Locate and identify every blood parasite.
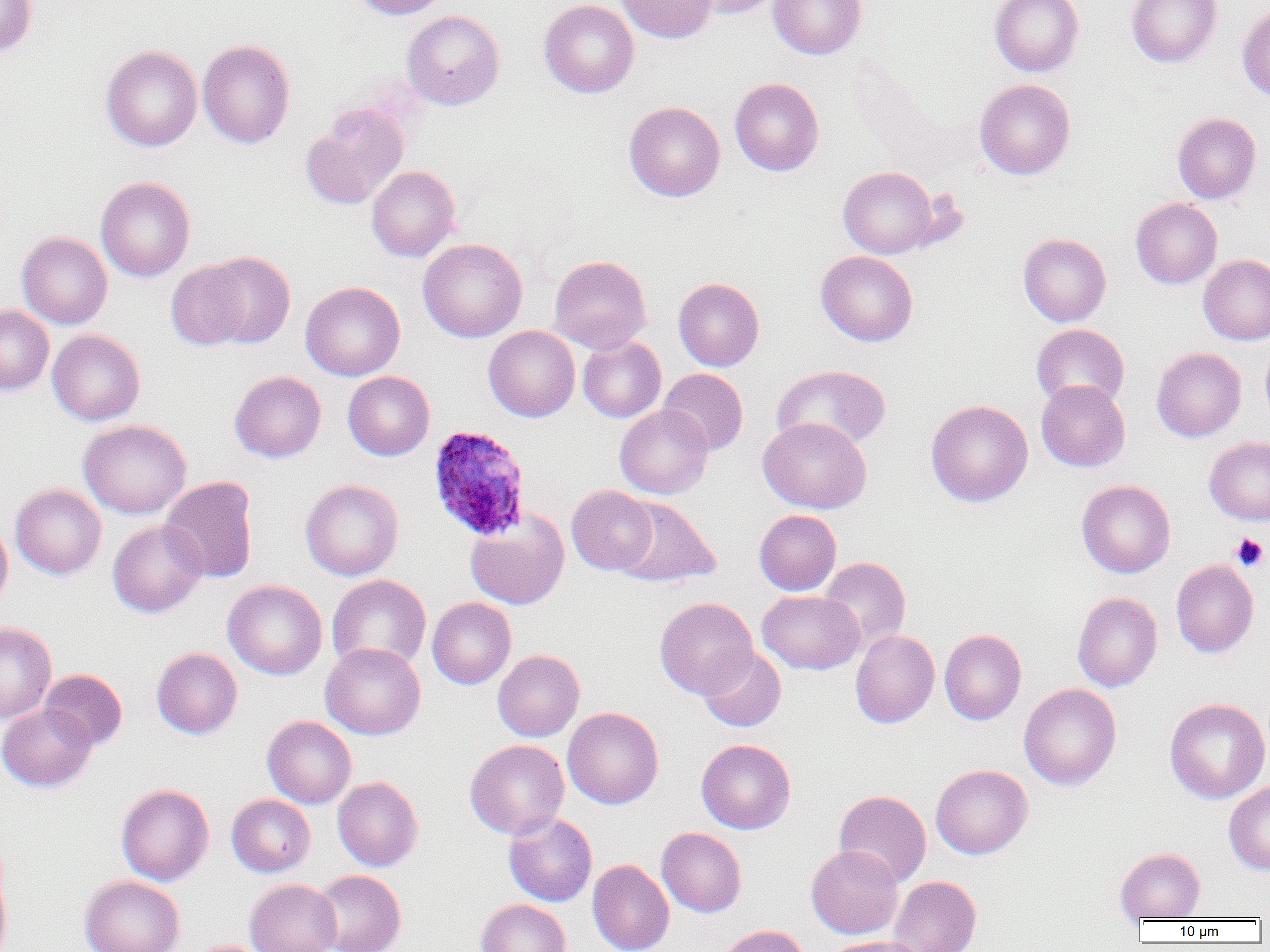
Approximate bounding boxes as (x1, y1, x2, y2) in pixels.
Plasmodium ovale-infected red blood cells: (427, 425, 532, 541).
No Plasmodium falciparum, Plasmodium malariae, Plasmodium vivax, Babesia divergens, or Trypanosoma brucei observed.

Summary:
  - Platelet locations: (1230, 532, 1269, 572)
  - Uninfected red blood cell locations: (0, 0, 37, 56), (351, 0, 451, 20), (539, 0, 639, 98), (615, 0, 717, 44), (684, 0, 783, 18), (768, 0, 866, 60), (989, 0, 1084, 77), (1126, 0, 1222, 68), (1237, 3, 1270, 102), (401, 10, 505, 110), (197, 39, 295, 149), (100, 44, 202, 152), (730, 77, 824, 176), (974, 78, 1075, 180), (624, 101, 725, 202), (301, 104, 409, 210), (1172, 112, 1261, 204), (367, 166, 460, 262), (838, 166, 941, 258), (95, 176, 195, 282), (1130, 198, 1222, 288), (16, 231, 112, 329), (1018, 233, 1111, 326), (418, 238, 527, 342), (816, 250, 918, 346), (196, 251, 296, 348), (1198, 254, 1270, 345), (549, 255, 651, 353), (165, 260, 255, 351), (673, 277, 764, 371), (300, 281, 405, 381), (0, 306, 54, 395), (1031, 324, 1129, 410), (483, 326, 580, 421), (47, 329, 145, 426), (578, 335, 666, 422), (1260, 340, 1270, 428), (1151, 346, 1246, 442), (772, 364, 891, 452), (658, 368, 748, 456), (229, 371, 326, 463), (343, 371, 435, 460), (1035, 379, 1130, 472), (925, 399, 1033, 507), (614, 405, 713, 499), (758, 417, 871, 513), (78, 419, 192, 519), (1204, 436, 1270, 525), (159, 476, 259, 583), (299, 478, 404, 581), (1076, 479, 1176, 578), (10, 483, 106, 579), (566, 485, 658, 575), (614, 497, 720, 587), (465, 509, 569, 609), (754, 509, 841, 595), (0, 518, 12, 610), (107, 520, 206, 617), (818, 556, 911, 653), (1171, 559, 1259, 658), (327, 574, 431, 673), (222, 579, 327, 680), (757, 590, 864, 675), (1072, 591, 1162, 692), (427, 597, 516, 689), (654, 597, 758, 699), (0, 622, 57, 723), (939, 629, 1026, 725), (850, 630, 939, 728), (320, 642, 426, 740), (697, 645, 787, 732), (151, 647, 242, 739), (482, 649, 575, 838), (493, 650, 584, 741), (39, 669, 127, 751), (1019, 683, 1122, 790), (1164, 697, 1270, 804), (0, 703, 97, 792), (562, 707, 664, 809), (262, 716, 356, 809), (465, 739, 569, 839), (696, 739, 796, 834), (930, 764, 1033, 859), (332, 776, 423, 871), (1224, 780, 1270, 874), (116, 783, 215, 885), (834, 789, 931, 888), (226, 794, 315, 877), (503, 812, 597, 907), (656, 827, 747, 917), (806, 845, 903, 939), (1115, 847, 1205, 922), (587, 858, 674, 952), (0, 864, 12, 952), (312, 870, 406, 952), (79, 875, 185, 952), (888, 875, 981, 952), (245, 878, 341, 952), (476, 898, 571, 952), (715, 924, 810, 952), (824, 936, 929, 952), (188, 940, 273, 952)
  - Slide-level diagnosis: Plasmodium ovale
  - Magnification: 1000x
  - Field of view: single
  - Image size: 1270×952 pixels
  - Preparation: thin blood smear
  - Modality: optical microscopy